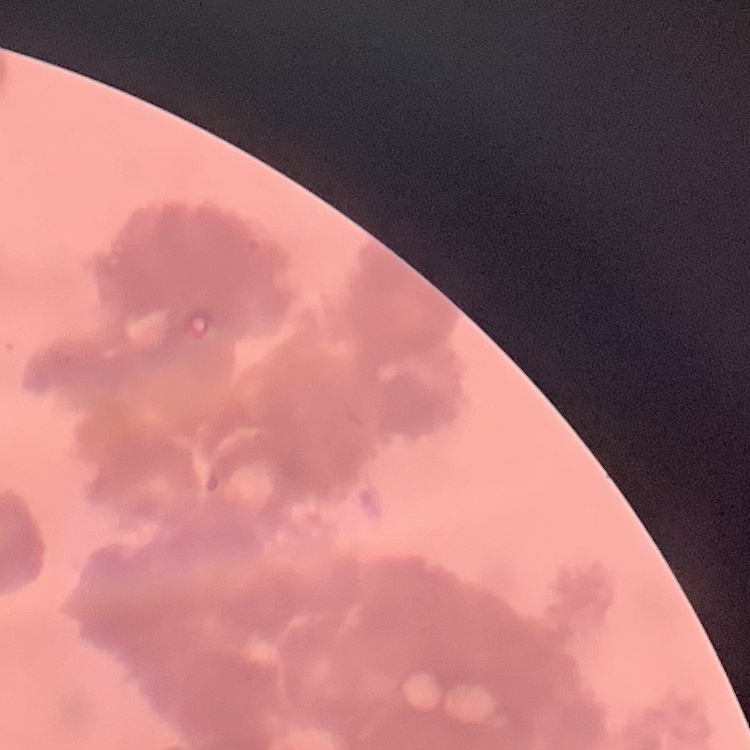
Summary:
  - Erythrocyte morphology: rouleaux formation
  - Preparation: thin blood film
  - Image type: square crop of a larger photomicrograph
  - Stain: Field's or Giemsa